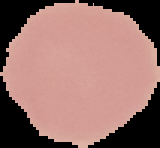
Summary:
  - Image type: segmented cell region with the area outside set to black
  - Preparation: thin blood smear
  - Image size: 160×148 pixels
  - Result: negative for Plasmodium parasites